Classify this cell by malaria status.
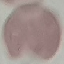

It is uninfected.

image type = automatically extracted cell patch, resized to 64 × 64 pixels
capture = smartphone camera at the microscope eyepiece
stain = Giemsa
preparation = thin smear